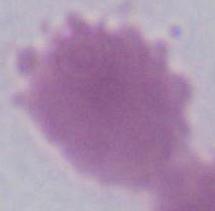
identification = red blood cell
modality = micrograph
magnification = 1000x